Locate and identify every blood parasite.
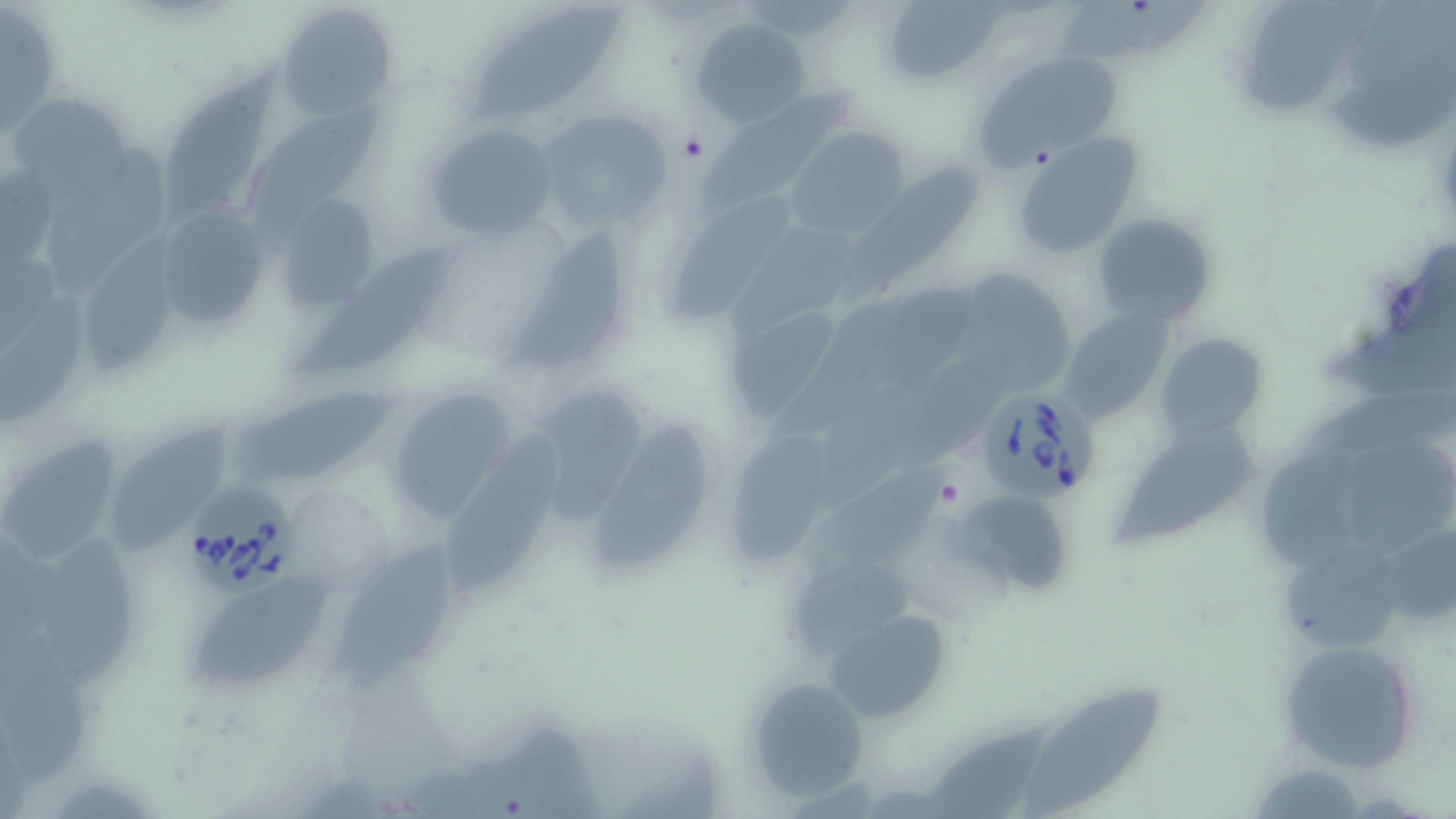
Approximate bounding boxes as (x1, y1, x2, y2) in pixels.
Babesia divergens-infected red blood cells: (975, 390, 1102, 504), (187, 481, 298, 596).
No Plasmodium falciparum, Plasmodium ovale, Plasmodium malariae, Plasmodium vivax, or Trypanosoma brucei observed.

Summary:
  - Platelet locations: (679, 133, 708, 162), (934, 478, 964, 509)
  - Uninfected red blood cell locations: (1054, 2, 1209, 67), (276, 4, 395, 121), (471, 5, 625, 117), (1249, 5, 1377, 118), (1, 7, 59, 134), (694, 17, 809, 126), (971, 51, 1123, 168), (162, 67, 279, 224), (700, 88, 861, 210), (9, 98, 139, 213), (248, 109, 383, 233), (539, 110, 671, 233), (427, 126, 556, 239), (787, 131, 908, 236), (1016, 136, 1144, 260), (39, 146, 173, 302), (850, 162, 983, 300), (281, 193, 377, 307), (660, 196, 795, 320), (159, 210, 273, 328), (1092, 212, 1218, 328), (727, 221, 873, 335), (504, 228, 623, 370), (82, 229, 182, 371), (298, 249, 458, 377), (964, 272, 1079, 391), (0, 295, 92, 430), (723, 304, 837, 416), (1059, 306, 1174, 425), (1157, 331, 1269, 440), (233, 385, 408, 488), (380, 387, 520, 528), (531, 389, 647, 523), (442, 422, 572, 597), (1114, 422, 1259, 546), (114, 425, 232, 558), (594, 425, 708, 574), (1337, 429, 1453, 551), (5, 430, 125, 571), (728, 433, 838, 570), (1255, 454, 1374, 572), (802, 464, 961, 570), (953, 488, 1071, 596), (338, 532, 453, 685), (37, 540, 143, 689), (1282, 548, 1397, 654), (796, 563, 916, 650), (189, 570, 332, 694), (822, 605, 958, 728), (1278, 638, 1427, 774), (746, 676, 871, 802), (1022, 690, 1164, 819), (914, 719, 1062, 819)
  - Slide-level diagnosis: Babesia divergens
  - Preparation: thin blood film
  - Magnification: 1000x
  - Modality: light microscopy
  - Field of view: single
  - Image size: 1456×819 pixels
  - Stain: May-Grünwald-Giemsa